Classify this cell by malaria status.
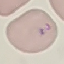

It is parasitized.

Summary:
  - Preparation: thin smear
  - Image type: cell patch, automatically extracted from a larger field of view and resized to 64 × 64 pixels
  - Capture: smartphone camera at the microscope eyepiece
  - Stain: Giemsa